State the preparation type.
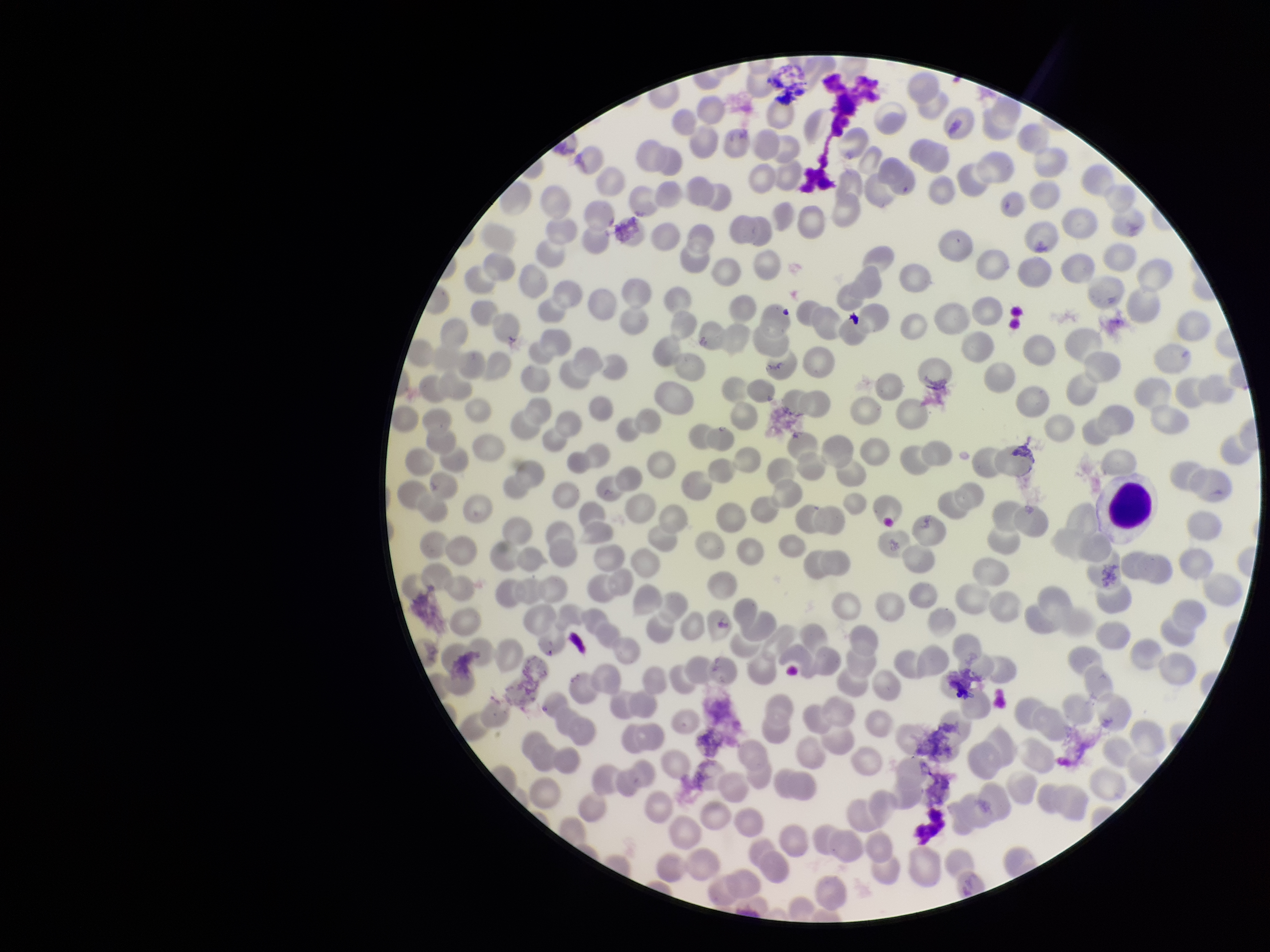

It is a thin blood smear.

stain = Giemsa
red blood cell count = 221
parasitized red blood cell count = 0
capture = smartphone photograph through the microscope eyepiece
parasitized red blood cells = none identified
image size = 1270×952 pixels
patient malaria status = negative
field of view = single